Locate every leukocyte (white blood cell).
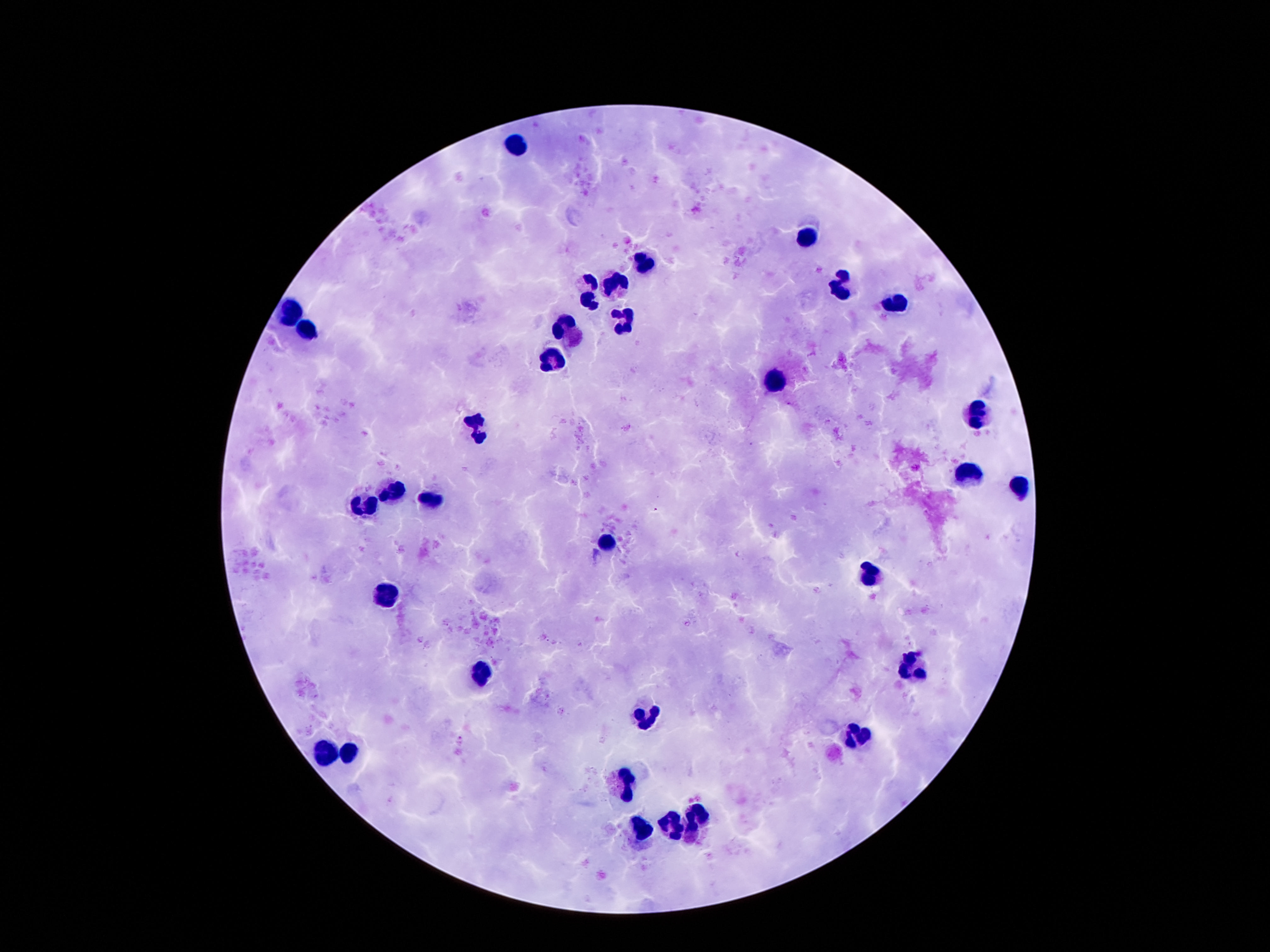
Approximate centers as (x, y) in pixels.
Leukocytes: (517, 145), (807, 238), (646, 262), (616, 283), (842, 283), (589, 284), (590, 301), (896, 301), (288, 314), (620, 321), (305, 329), (570, 330), (552, 363), (778, 380), (977, 416), (476, 427), (969, 474), (1018, 489), (395, 492), (429, 496), (362, 505), (607, 541), (870, 576), (387, 594), (914, 665), (477, 674), (645, 717), (857, 736), (351, 754), (322, 755), (624, 782), (700, 821), (671, 829), (641, 831).

field of view = one from this slide
patient malaria status = uninfected
magnification = 100x
stain = Giemsa
image size = 1270×952 pixels
capture = smartphone camera through the microscope eyepiece
preparation = thick blood smear